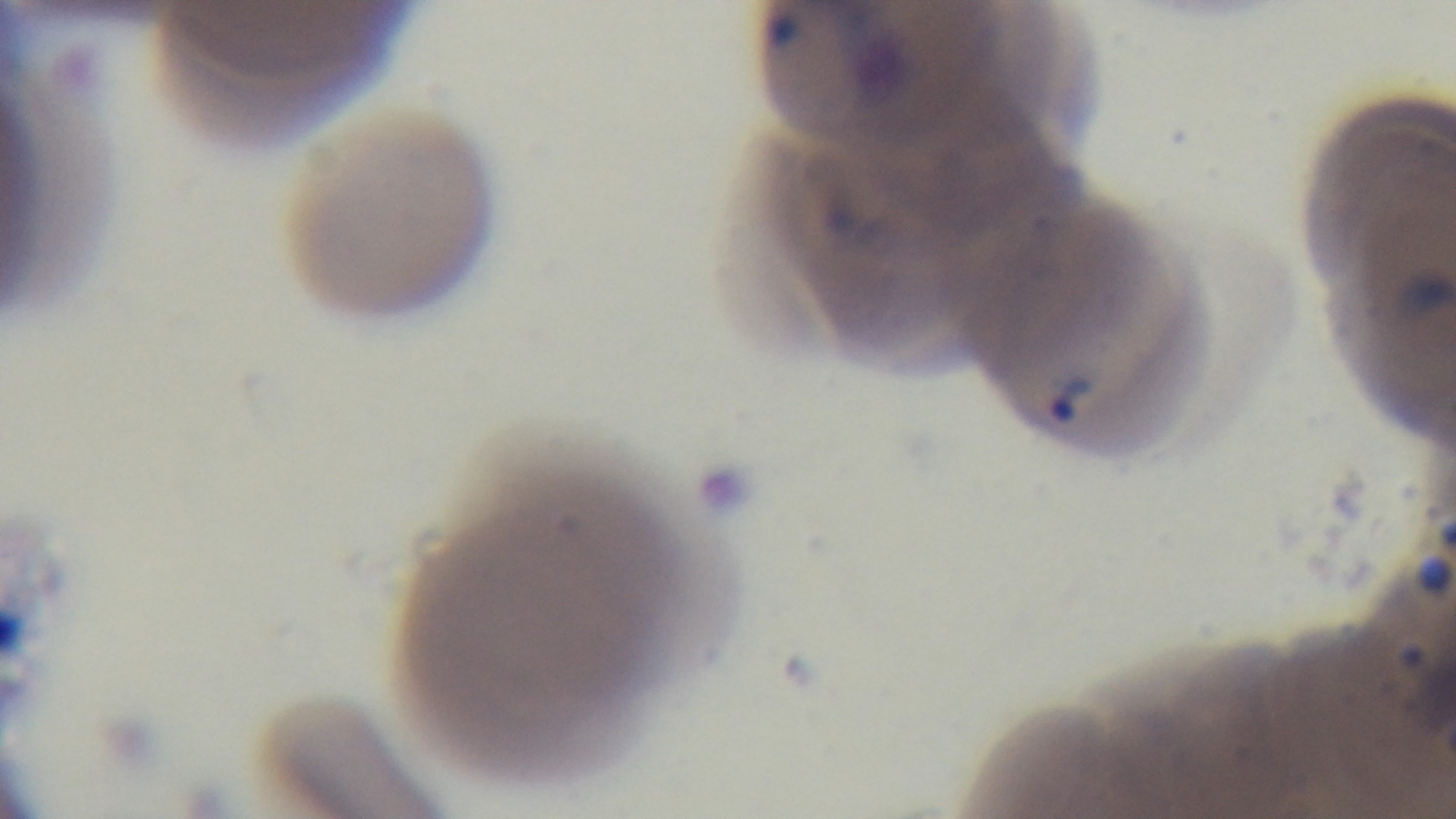 Single field of view. Photomicrograph. Captured with a mounted 4K digital camera. Preparation: thin blood film. Oil-immersion objective, 100x. Malaria status: infected. Giemsa stain.